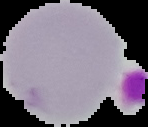
Result: no Plasmodium parasites detected. Image is 148×127 pixels. From a thin blood film. Cell region segmented out of the field of view; the surrounding area is masked to black.